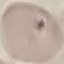

Summary:
  - Malaria status: uninfected
  - Image type: cell patch, automatically extracted from a larger field of view and resized to 64 × 64 pixels
  - Capture: smartphone through the microscope eyepiece
  - Stain: Giemsa
  - Preparation: thin blood film